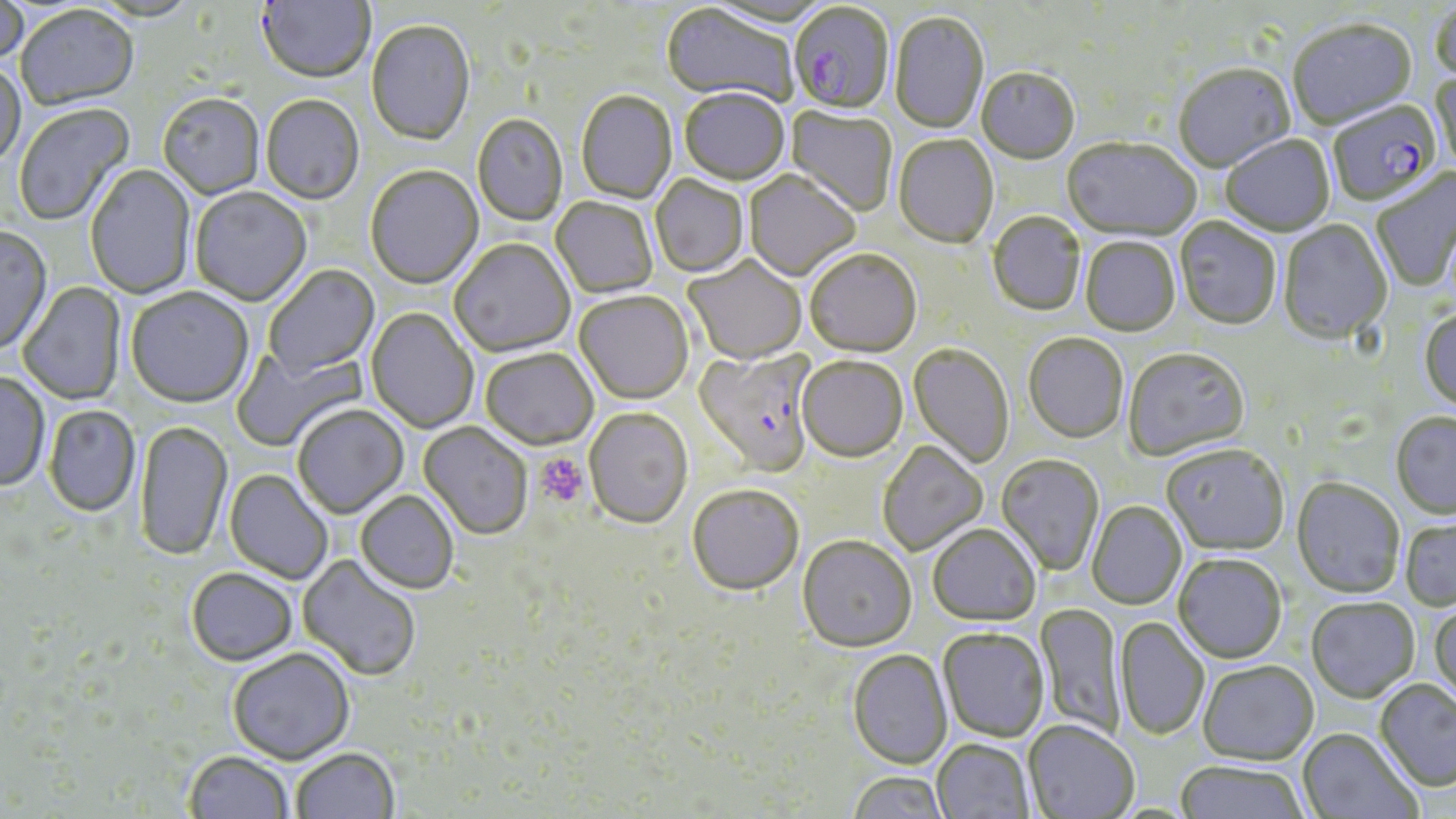

slide-level diagnosis = Plasmodium falciparum
preparation = thin blood film
platelet locations = approximate bounding boxes as named x1/y1/x2/y2 corners in pixels: (x1=535, y1=452, x2=589, y2=507)
Plasmodium falciparum-infected red blood cell locations = approximate bounding boxes as named x1/y1/x2/y2 corners in pixels: (x1=787, y1=5, x2=895, y2=116), (x1=1328, y1=101, x2=1442, y2=209), (x1=693, y1=348, x2=818, y2=479)
field of view = one of a larger specimen
magnification = 1000x
image size = 1456×819 pixels
stain = May-Grünwald-Giemsa
uninfected red blood cell locations = approximate bounding boxes as named x1/y1/x2/y2 corners in pixels: (x1=256, y1=0, x2=374, y2=85), (x1=0, y1=2, x2=29, y2=68), (x1=1429, y1=3, x2=1456, y2=87), (x1=661, y1=4, x2=797, y2=108), (x1=16, y1=7, x2=139, y2=112), (x1=890, y1=12, x2=989, y2=136), (x1=366, y1=21, x2=475, y2=148), (x1=1288, y1=21, x2=1418, y2=132), (x1=0, y1=63, x2=26, y2=171), (x1=1173, y1=65, x2=1295, y2=175), (x1=1430, y1=68, x2=1456, y2=178), (x1=976, y1=69, x2=1080, y2=166), (x1=679, y1=90, x2=789, y2=187), (x1=576, y1=92, x2=677, y2=205), (x1=158, y1=95, x2=265, y2=200), (x1=261, y1=96, x2=364, y2=206), (x1=13, y1=103, x2=136, y2=228), (x1=785, y1=106, x2=897, y2=217), (x1=472, y1=115, x2=567, y2=227), (x1=893, y1=136, x2=999, y2=250), (x1=1221, y1=136, x2=1335, y2=238), (x1=1061, y1=139, x2=1201, y2=244), (x1=85, y1=165, x2=196, y2=300), (x1=365, y1=167, x2=483, y2=290), (x1=1371, y1=168, x2=1456, y2=292), (x1=744, y1=171, x2=860, y2=283), (x1=650, y1=176, x2=749, y2=278), (x1=190, y1=188, x2=312, y2=307), (x1=551, y1=197, x2=658, y2=299), (x1=988, y1=213, x2=1086, y2=317), (x1=1174, y1=218, x2=1281, y2=332), (x1=1277, y1=221, x2=1393, y2=347), (x1=0, y1=227, x2=53, y2=355), (x1=1080, y1=237, x2=1180, y2=337), (x1=449, y1=239, x2=575, y2=359), (x1=805, y1=251, x2=921, y2=360), (x1=683, y1=257, x2=806, y2=366), (x1=264, y1=265, x2=380, y2=380), (x1=17, y1=281, x2=126, y2=406), (x1=125, y1=288, x2=254, y2=409), (x1=574, y1=292, x2=694, y2=406), (x1=366, y1=308, x2=478, y2=433), (x1=1419, y1=310, x2=1456, y2=414), (x1=1023, y1=335, x2=1129, y2=445), (x1=231, y1=343, x2=367, y2=452), (x1=908, y1=345, x2=1014, y2=469), (x1=480, y1=349, x2=598, y2=452), (x1=1123, y1=350, x2=1250, y2=463), (x1=797, y1=358, x2=907, y2=465), (x1=0, y1=372, x2=49, y2=492), (x1=44, y1=405, x2=140, y2=518), (x1=292, y1=406, x2=409, y2=520), (x1=584, y1=409, x2=693, y2=530), (x1=1391, y1=413, x2=1456, y2=520), (x1=134, y1=420, x2=233, y2=562), (x1=418, y1=422, x2=533, y2=541), (x1=878, y1=441, x2=988, y2=556), (x1=1161, y1=445, x2=1289, y2=557), (x1=996, y1=455, x2=1104, y2=577), (x1=224, y1=470, x2=333, y2=584), (x1=1291, y1=479, x2=1406, y2=600), (x1=687, y1=487, x2=804, y2=598), (x1=355, y1=492, x2=459, y2=595), (x1=1087, y1=501, x2=1187, y2=611), (x1=1400, y1=519, x2=1456, y2=612), (x1=928, y1=526, x2=1041, y2=628), (x1=797, y1=537, x2=916, y2=655), (x1=297, y1=555, x2=421, y2=682), (x1=1173, y1=556, x2=1287, y2=665), (x1=188, y1=567, x2=298, y2=667), (x1=1306, y1=600, x2=1420, y2=705), (x1=1035, y1=603, x2=1125, y2=738), (x1=1428, y1=604, x2=1456, y2=710), (x1=1114, y1=617, x2=1209, y2=742), (x1=938, y1=629, x2=1049, y2=743), (x1=228, y1=648, x2=354, y2=765), (x1=847, y1=650, x2=952, y2=771), (x1=1198, y1=662, x2=1319, y2=768), (x1=1374, y1=680, x2=1456, y2=792), (x1=1023, y1=722, x2=1138, y2=819), (x1=1298, y1=728, x2=1422, y2=819), (x1=931, y1=741, x2=1035, y2=819), (x1=291, y1=748, x2=399, y2=819), (x1=184, y1=750, x2=294, y2=819), (x1=1174, y1=763, x2=1309, y2=819), (x1=847, y1=773, x2=948, y2=819)
modality = light microscopy